Classify this cell by malaria status.
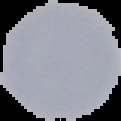

Uninfected.

preparation = thin blood film
image size = 121×121 pixels
image type = cell region segmented out of the field of view; surrounding area masked to black